Locate every leukocyte (white blood cell).
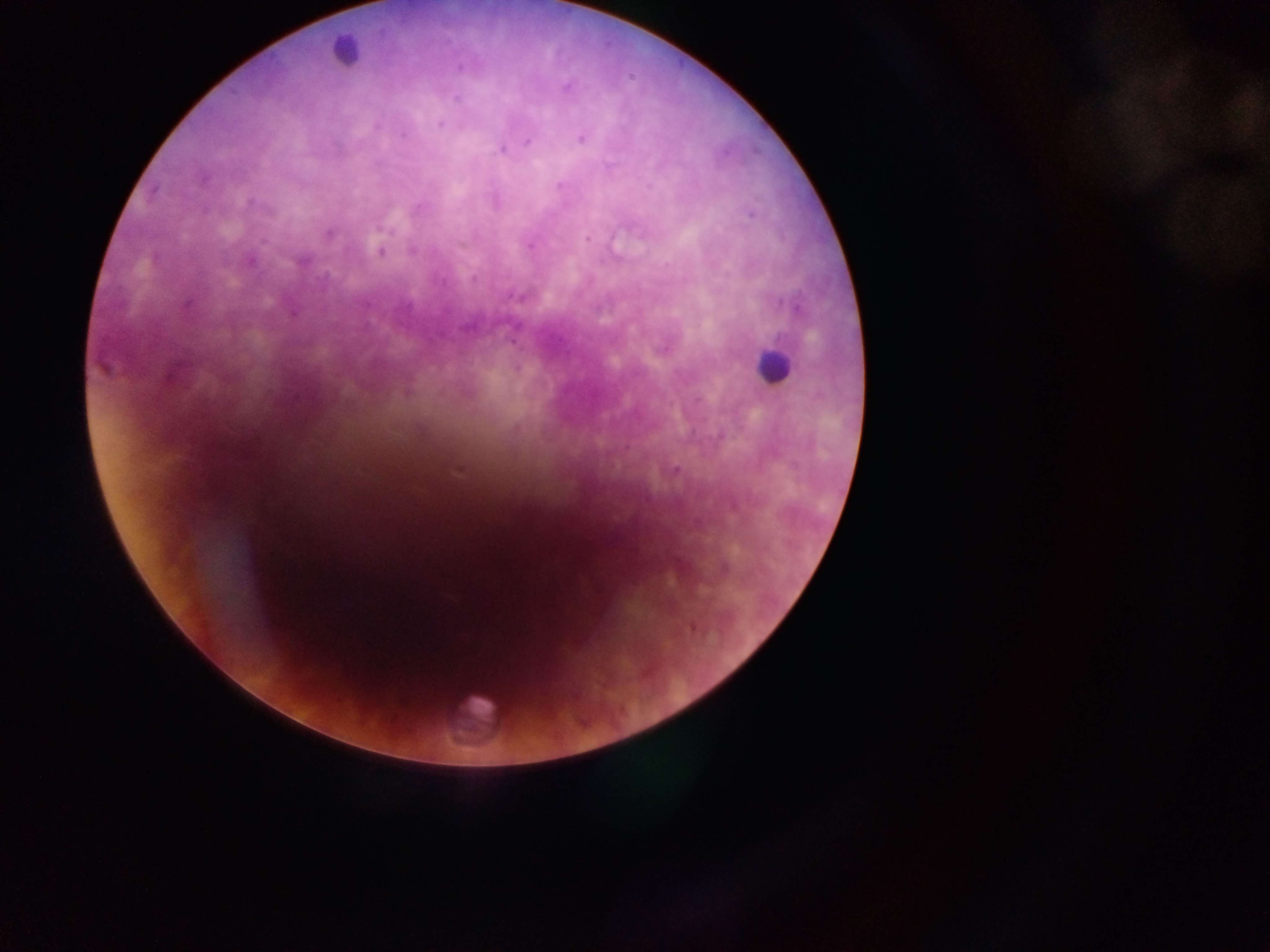

Approximate centers as [x, y] in pixels.
Leukocytes: [343, 51], [771, 364], [475, 718].

Plasmodium parasite locations: [459, 67], [630, 77], [566, 87], [457, 100], [440, 124], [403, 135], [581, 139], [528, 141], [502, 150], [559, 185], [154, 190], [419, 206], [750, 214], [328, 234], [587, 238], [530, 246], [381, 251], [412, 251], [473, 278], [515, 297], [513, 340], [103, 367], [698, 400], [516, 428], [459, 470], [675, 470], [733, 504], [724, 568], [692, 628]. Thick blood smear. Single field of view. Mobile-phone photograph taken through the microscope. Image is 1270×952 pixels. Collected in Ghana.